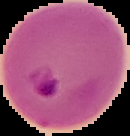
preparation = thin blood film
image size = 130×136 pixels
result = Plasmodium parasites identified
image type = segmented cell region with the area outside set to black